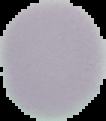

From a thin blood film. Result: no malaria parasites detected. The area outside the segmented cell region is set to black. Image is 106×121 pixels.